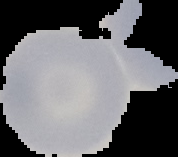

image_size: 178×157 pixels
image_type: cell region segmented out of the field of view; surrounding area masked to black
preparation: thin blood film
malaria_status: uninfected